Name the cell type shown.
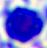

A leukocyte.

Summary:
  - Modality: micrograph
  - Magnification: 400x